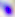
Summary:
  - Modality: photomicrograph
  - Identification: Toxoplasma gondii
  - Magnification: 400x